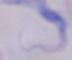
{
  "modality": "micrograph",
  "magnification": "1000x",
  "identification": "trypanosome"
}